Assess this cell for malaria.
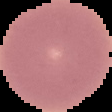

Uninfected.

Image is 112×112 pixels. From a thin blood film. Cell region segmented out of the field of view; the surrounding area is masked to black.